Locate every leukocyte (white blood cell).
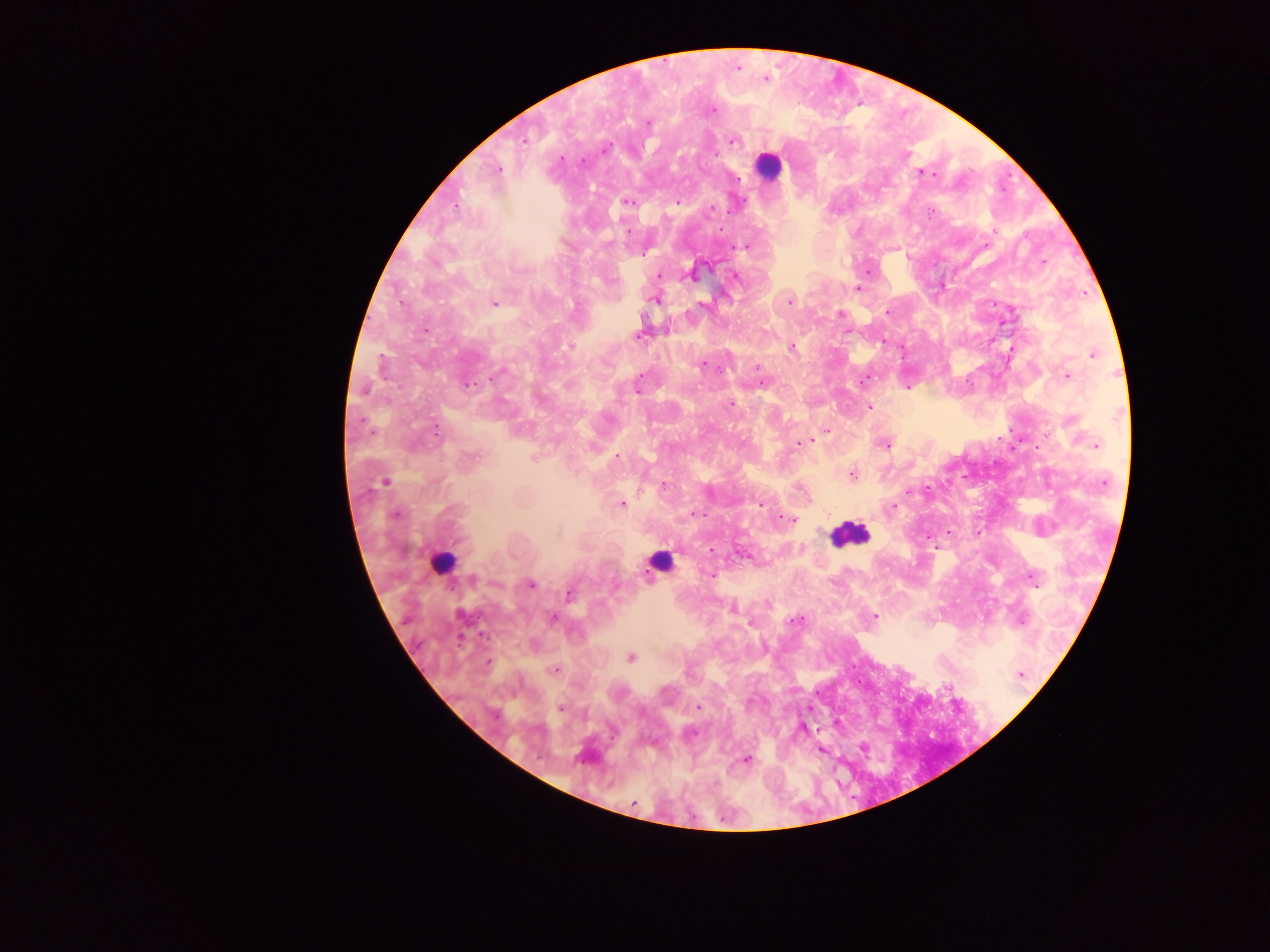
Approximate centers as [x, y] in pixels.
Leukocytes: [769, 166], [848, 534], [659, 562], [441, 563].

{
  "image_size": "1270×952 pixels",
  "field_of_view": "single",
  "country": "Ghana",
  "preparation": "thick blood film",
  "capture": "mobile-phone photograph through a microscope",
  "plasmodium_parasite_locations": "approximate centers as [x, y] in pixels: [738, 68], [765, 79], [712, 110], [648, 122], [523, 140], [733, 140], [605, 148], [715, 154], [561, 158], [583, 161], [497, 170], [920, 172], [738, 179], [627, 202], [678, 202], [456, 207], [711, 209], [628, 231], [607, 244], [741, 246], [659, 275], [692, 276], [736, 276], [611, 280], [858, 289], [656, 300], [789, 302], [493, 303], [888, 312], [841, 314], [425, 329], [638, 336], [883, 341], [569, 346], [792, 347], [1093, 355], [704, 364], [758, 369], [497, 375], [640, 375], [1067, 376], [863, 380], [761, 383], [468, 385], [907, 386], [364, 390], [731, 404], [870, 407], [827, 430], [436, 432], [813, 441], [802, 442], [886, 445], [1096, 446], [617, 457], [852, 475], [1104, 482], [383, 483], [663, 485], [909, 491], [810, 500], [760, 503], [621, 504], [894, 506], [695, 513], [395, 515], [789, 520], [712, 550], [744, 555], [711, 575], [474, 579], [1033, 579], [531, 584], [569, 593], [733, 609], [874, 616], [553, 618], [794, 620], [1022, 621], [462, 639], [631, 658], [488, 662], [554, 670], [1021, 675], [698, 707], [560, 709], [494, 715], [690, 732], [745, 760], [633, 802]"
}